Assess the morphology of the red blood cells.
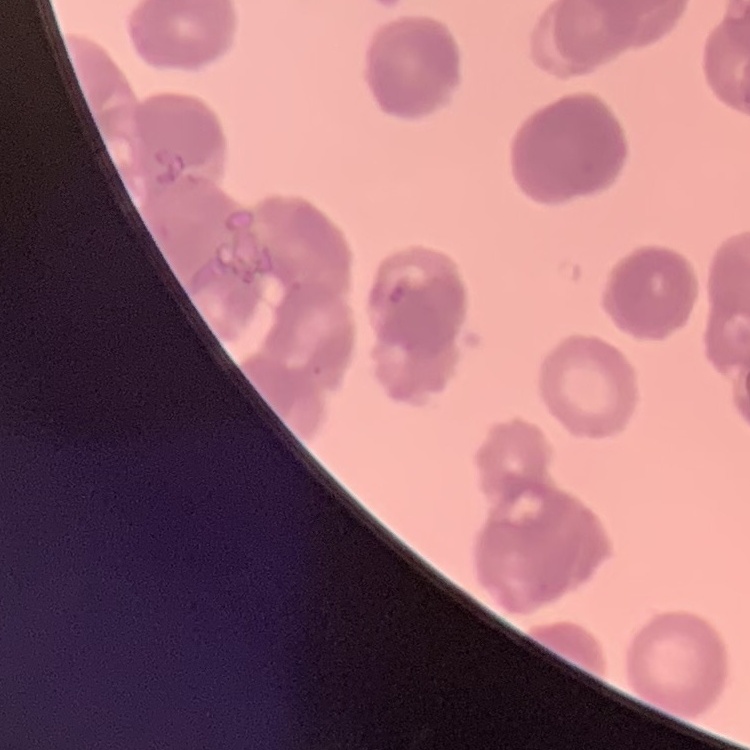
Rouleaux formation.

Field's or Giemsa stain. Square crop of a larger photomicrograph. Thin peripheral smear.